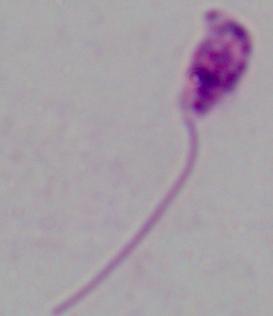

identification: Leishmania
magnification: 1000x
modality: micrograph